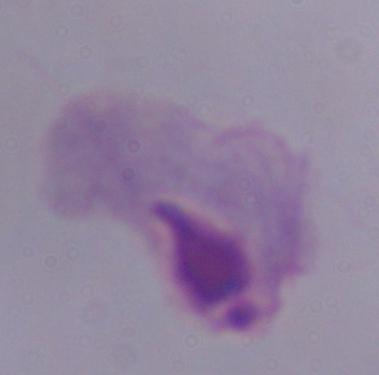

Summary:
  - Identification: trichomonad
  - Modality: photomicrograph
  - Magnification: 1000x